Classify this cell by malaria status.
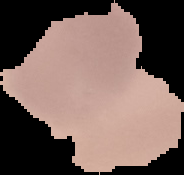

It is uninfected.

Summary:
  - Preparation: thin blood film
  - Image size: 184×175 pixels
  - Image type: cell region segmented out of the field of view; surrounding area masked to black